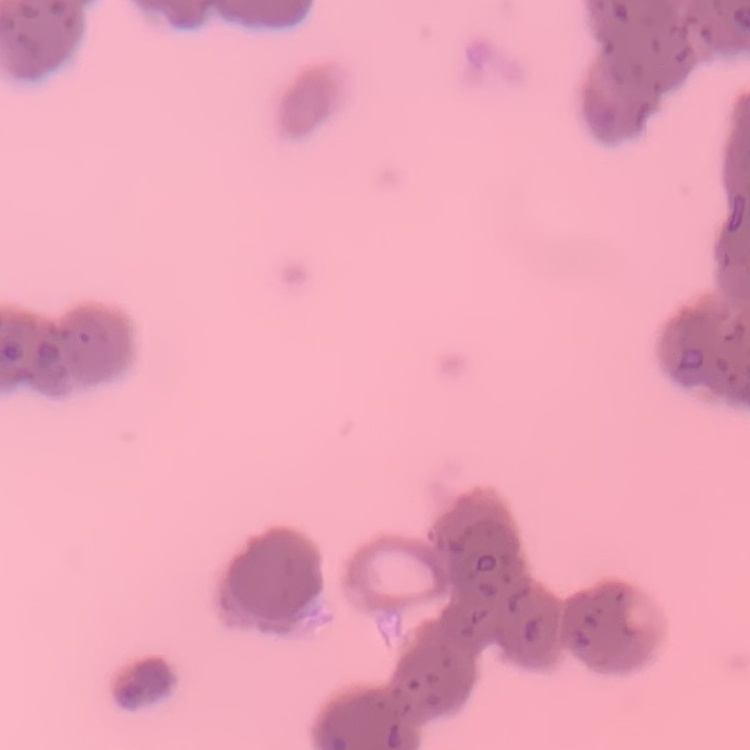
red_blood_cell_morphology: rouleaux formation
stain: Field's or Giemsa
preparation: thin blood smear
image_type: square crop of a larger photomicrograph